Outline each blood parasite and name the species.
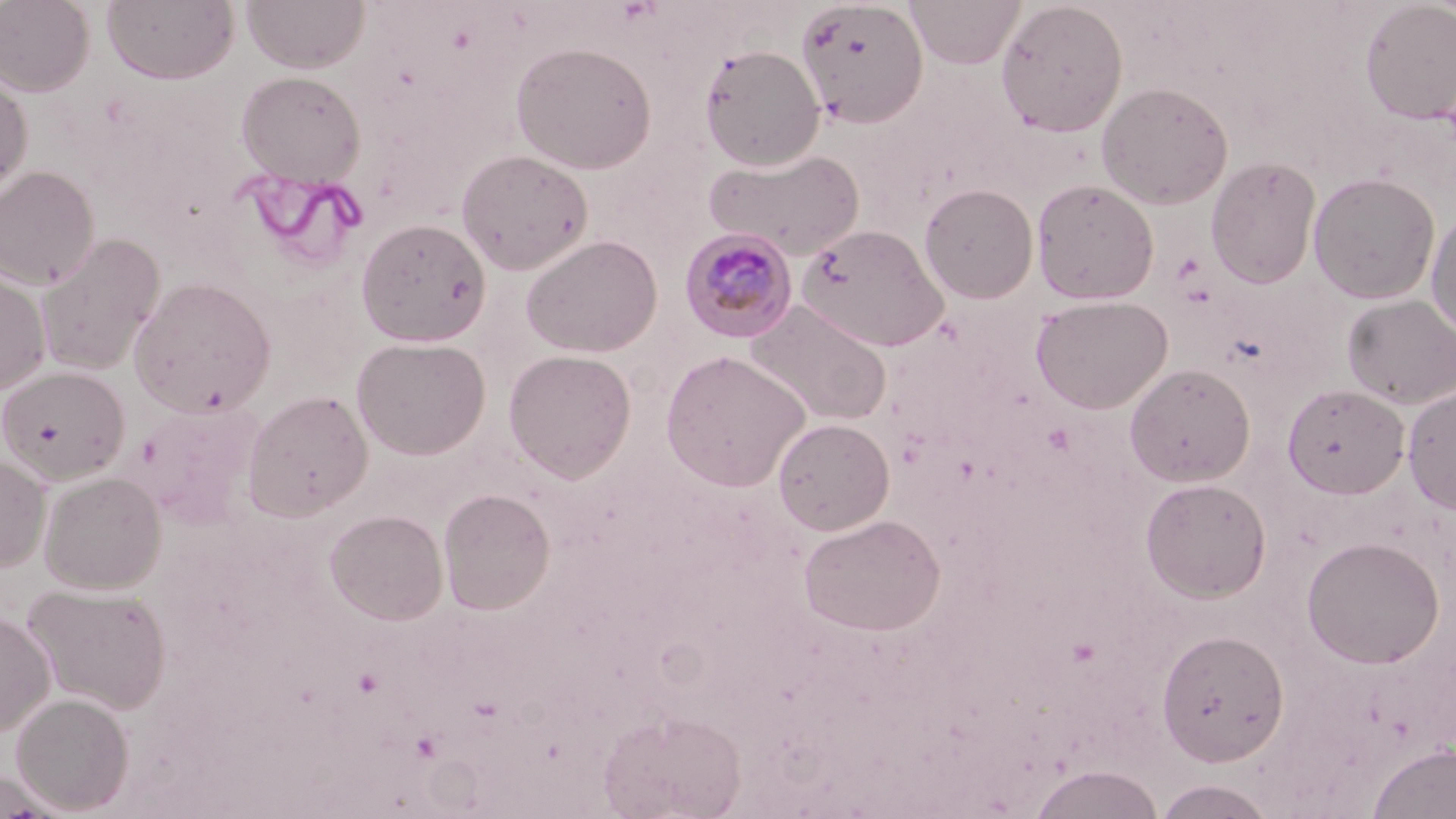
Approximate bounding boxes as (x1,y1)-(x2,y2) corner pairs in pixels.
Plasmodium malariae-infected red blood cells: (680,227)-(799,343).
No Plasmodium falciparum, Plasmodium ovale, Plasmodium vivax, Babesia divergens, or Trypanosoma brucei observed.

slide-level diagnosis = Plasmodium malariae
uninfected red blood cell locations = approximate bounding boxes as (x1,y1)-(x2,y2) corner pairs in pixels: (0,0)-(95,96), (101,0)-(239,85), (242,0)-(370,73), (905,0)-(1026,68), (795,1)-(928,128), (995,1)-(1129,137), (1359,1)-(1456,124), (510,41)-(657,174), (699,45)-(825,170), (236,70)-(366,186), (0,71)-(33,197), (1096,81)-(1233,209), (704,147)-(864,260), (456,148)-(593,275), (1206,155)-(1321,289), (0,165)-(99,291), (1308,172)-(1440,304), (1031,179)-(1159,305), (919,183)-(1039,303), (1426,208)-(1456,341), (355,218)-(491,346), (796,223)-(948,351), (35,232)-(165,377), (520,234)-(662,357), (0,266)-(51,396), (129,277)-(277,417), (1341,294)-(1456,408), (1030,295)-(1172,413), (744,299)-(892,426), (351,335)-(491,460), (502,349)-(637,482), (661,350)-(810,492), (1125,363)-(1255,487), (0,365)-(130,484), (1403,383)-(1456,513), (1282,384)-(1410,498), (242,389)-(374,520), (772,417)-(894,535), (0,454)-(52,572), (39,470)-(167,594), (1139,477)-(1272,602), (438,488)-(555,615), (324,508)-(448,625), (798,514)-(945,636), (1302,535)-(1445,669), (24,583)-(172,714), (0,610)-(55,737), (1155,627)-(1289,766), (11,692)-(134,814), (598,709)-(745,819), (1367,742)-(1456,819), (1028,764)-(1164,819), (1150,778)-(1279,818)
modality = optical microscopy
preparation = thin blood film
stain = May-Grünwald-Giemsa
magnification = 1000x
field of view = single
image size = 1456×819 pixels